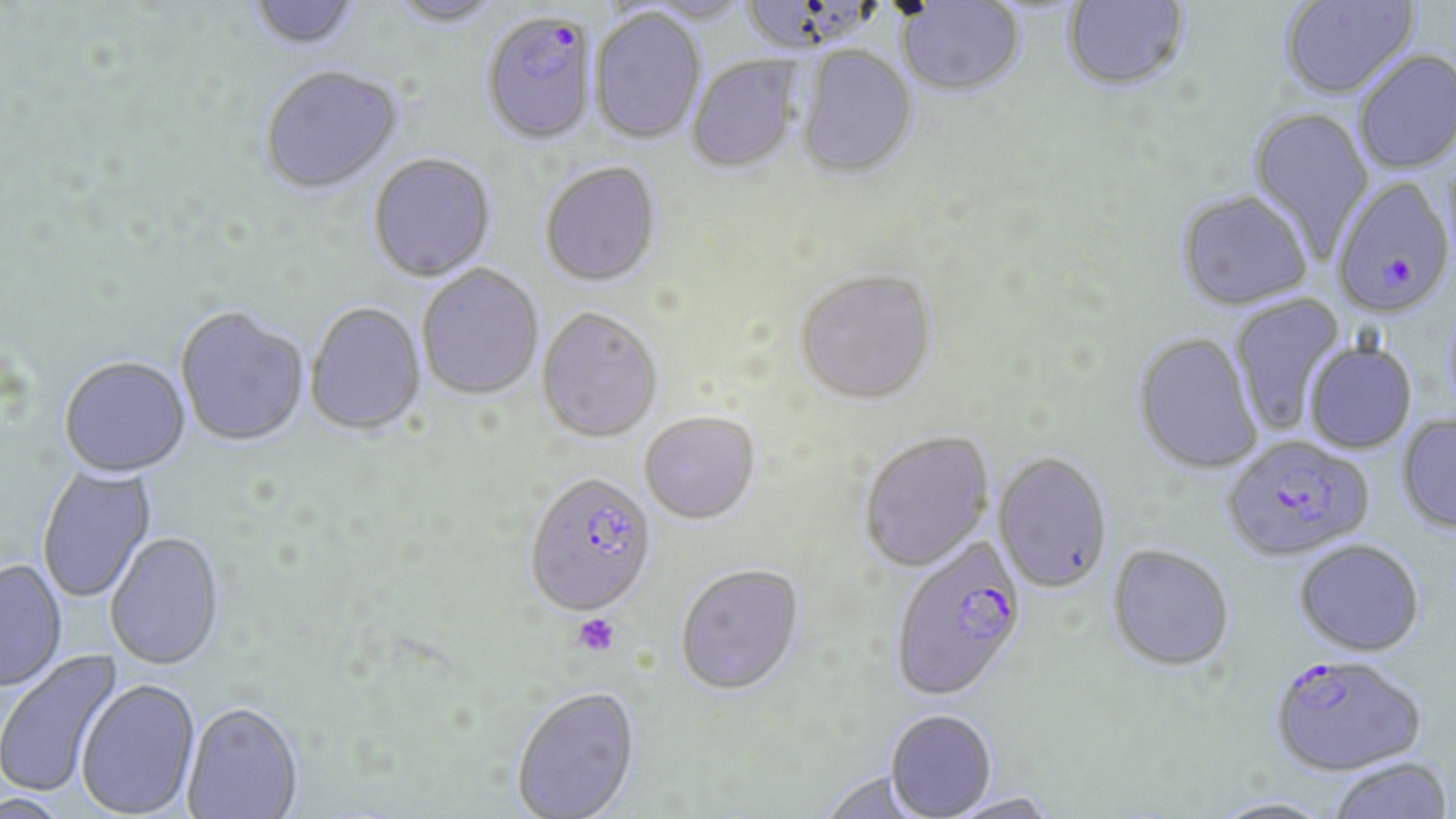

Summary:
  - Coordinate format: approximate bounding boxes as [x1, y1, x2, y2] in pixels
  - Plasmodium falciparum-infected red blood cell locations: [480, 15, 598, 147], [1332, 177, 1455, 318], [1222, 436, 1374, 563], [524, 475, 658, 620], [896, 533, 1027, 700], [1275, 656, 1422, 774]
  - Uninfected red blood cell locations: [384, 0, 507, 29], [645, 0, 753, 26], [744, 0, 885, 57], [1059, 0, 1193, 95], [1278, 0, 1419, 101], [247, 1, 364, 54], [895, 1, 1027, 100], [589, 9, 706, 146], [795, 46, 919, 180], [1353, 50, 1456, 174], [687, 57, 803, 175], [259, 67, 404, 198], [1247, 108, 1375, 259], [368, 154, 497, 284], [539, 164, 663, 290], [1175, 191, 1313, 312], [416, 266, 544, 401], [794, 272, 938, 408], [1228, 292, 1348, 436], [305, 304, 426, 438], [175, 309, 309, 450], [536, 309, 663, 445], [1131, 333, 1263, 476], [1304, 342, 1417, 454], [58, 358, 191, 481], [639, 414, 761, 527], [1396, 414, 1456, 535], [858, 432, 994, 574], [992, 452, 1113, 595], [37, 465, 157, 603], [105, 533, 226, 674], [1294, 540, 1426, 656], [1106, 544, 1235, 672], [0, 560, 68, 694], [676, 566, 805, 699], [0, 648, 124, 797], [76, 681, 201, 818], [511, 689, 642, 819], [182, 706, 304, 818], [885, 710, 998, 819], [1326, 757, 1454, 818], [818, 770, 928, 818], [2, 792, 69, 819], [943, 793, 1061, 819], [1204, 795, 1340, 819]
  - Platelet locations: [572, 613, 620, 658]
  - Slide-level diagnosis: Plasmodium falciparum
  - Image size: 1456×819 pixels
  - Stain: May-Grünwald-Giemsa
  - Preparation: thin blood smear
  - Field of view: one of a larger specimen
  - Magnification: 1000x
  - Modality: optical microscopy